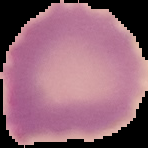

{
  "image_type": "segmented cell region on a black background",
  "preparation": "thin blood smear",
  "malaria_status": "uninfected",
  "image_size": "148×148 pixels"
}